Name the cell type shown.
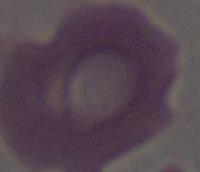
This is an erythrocyte.

Micrograph. Captured at 1000x magnification.